Report the malaria status of this cell.
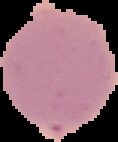
It is uninfected.

From a thin blood smear. Image is 118×142 pixels. Segmented cell region on a black background.